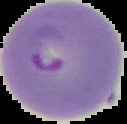
preparation = thin blood smear
image type = segmented cell region with the area outside set to black
malaria status = parasitized
image size = 127×124 pixels